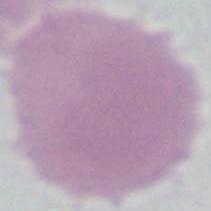
modality: photomicrograph
identification: red blood cell
magnification: 1000x